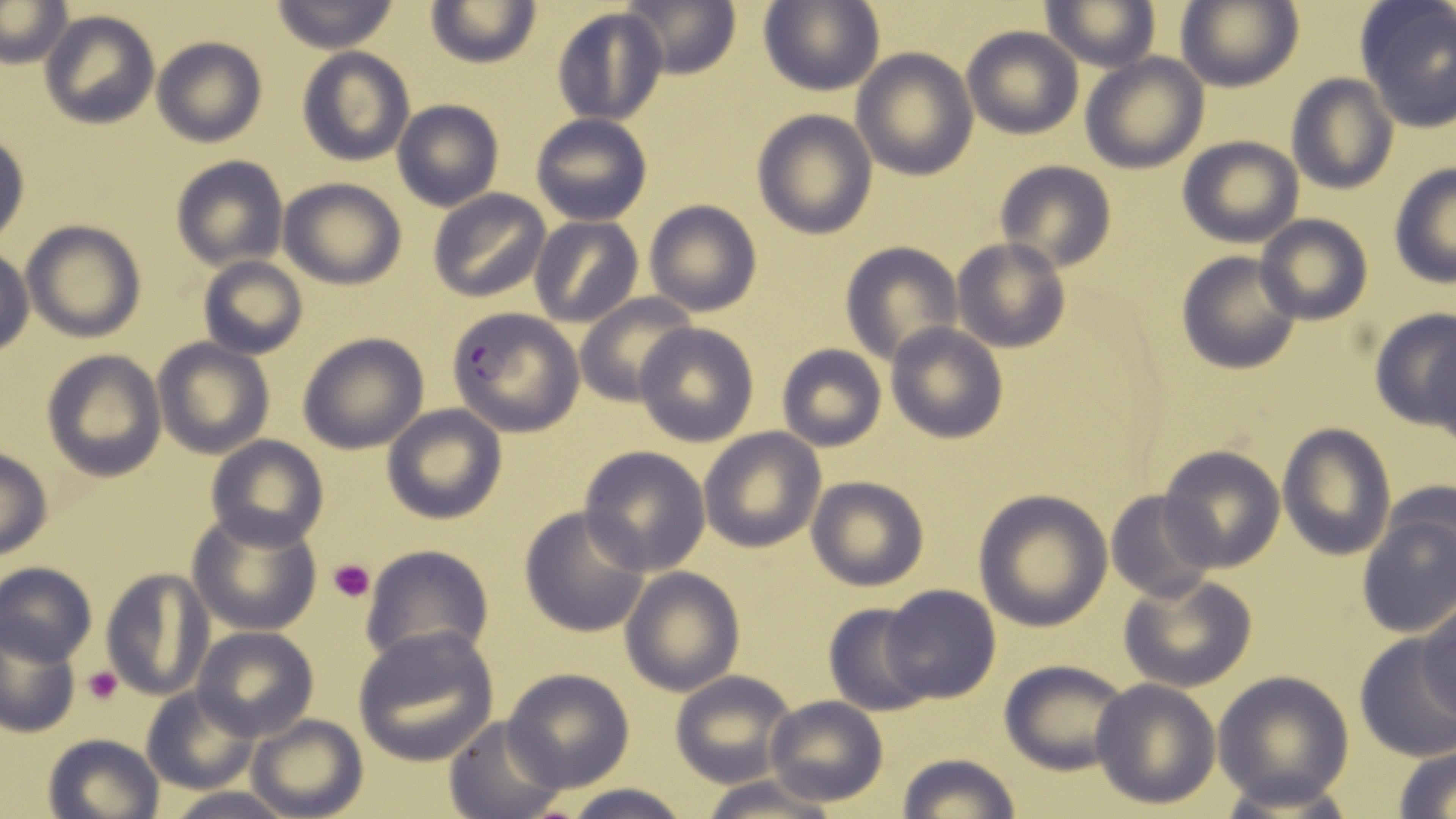
Summary:
  - Coordinate format: approximate bounding boxes as [x1, y1, x2, y2] in pixels
  - Platelet locations: [328, 559, 375, 603], [83, 664, 123, 706]
  - Uninfected red blood cell locations: [0, 0, 73, 67], [268, 0, 400, 52], [618, 0, 742, 79], [1177, 0, 1302, 92], [426, 1, 541, 69], [759, 1, 884, 97], [1042, 1, 1160, 72], [1355, 1, 1456, 132], [551, 8, 669, 127], [40, 10, 159, 129], [962, 26, 1083, 139], [151, 36, 267, 147], [296, 47, 414, 166], [852, 47, 978, 179], [1081, 53, 1207, 173], [1286, 72, 1399, 193], [391, 100, 504, 211], [751, 108, 878, 239], [529, 113, 653, 225], [0, 125, 31, 244], [1177, 135, 1304, 248], [170, 157, 288, 270], [994, 161, 1115, 275], [1388, 162, 1456, 287], [279, 178, 405, 289], [428, 188, 551, 304], [644, 200, 761, 315], [1255, 214, 1372, 326], [528, 217, 644, 329], [20, 219, 146, 341], [952, 240, 1070, 353], [840, 242, 963, 365], [0, 247, 33, 358], [1176, 250, 1304, 374], [197, 255, 307, 360], [575, 293, 699, 406], [1369, 309, 1455, 429], [635, 323, 759, 446], [886, 323, 1008, 443], [1426, 331, 1456, 458], [296, 333, 429, 455], [152, 339, 274, 458], [776, 344, 885, 451], [42, 351, 166, 480], [381, 404, 507, 523], [1277, 423, 1395, 560], [699, 428, 826, 552], [205, 436, 327, 551], [1158, 444, 1287, 572], [579, 446, 710, 575], [0, 447, 52, 560], [806, 475, 928, 591], [1105, 489, 1221, 604], [973, 490, 1113, 632], [1355, 504, 1456, 639], [518, 505, 652, 638], [188, 510, 322, 636], [361, 544, 492, 667], [2, 562, 97, 666], [620, 565, 745, 697], [100, 568, 212, 701], [1119, 572, 1258, 692], [880, 583, 1001, 704], [823, 602, 933, 717], [1419, 604, 1455, 720], [0, 625, 81, 738], [194, 627, 319, 741], [352, 627, 499, 766], [1354, 634, 1456, 762], [998, 658, 1133, 773], [502, 668, 634, 791], [669, 671, 796, 787], [1213, 671, 1353, 808], [1089, 680, 1219, 809], [142, 687, 260, 793], [765, 694, 887, 807], [246, 713, 366, 819], [443, 716, 563, 816], [42, 732, 164, 819], [1391, 744, 1456, 818], [895, 752, 1020, 818], [699, 775, 839, 819], [555, 786, 694, 819], [162, 788, 299, 819]
  - Plasmodium falciparum-infected red blood cell locations: [447, 306, 585, 436]
  - Slide-level diagnosis: Plasmodium falciparum
  - Stain: May-Grünwald-Giemsa
  - Field of view: single
  - Preparation: thin blood smear
  - Modality: light microscopy
  - Image size: 1456×819 pixels
  - Magnification: 1000x